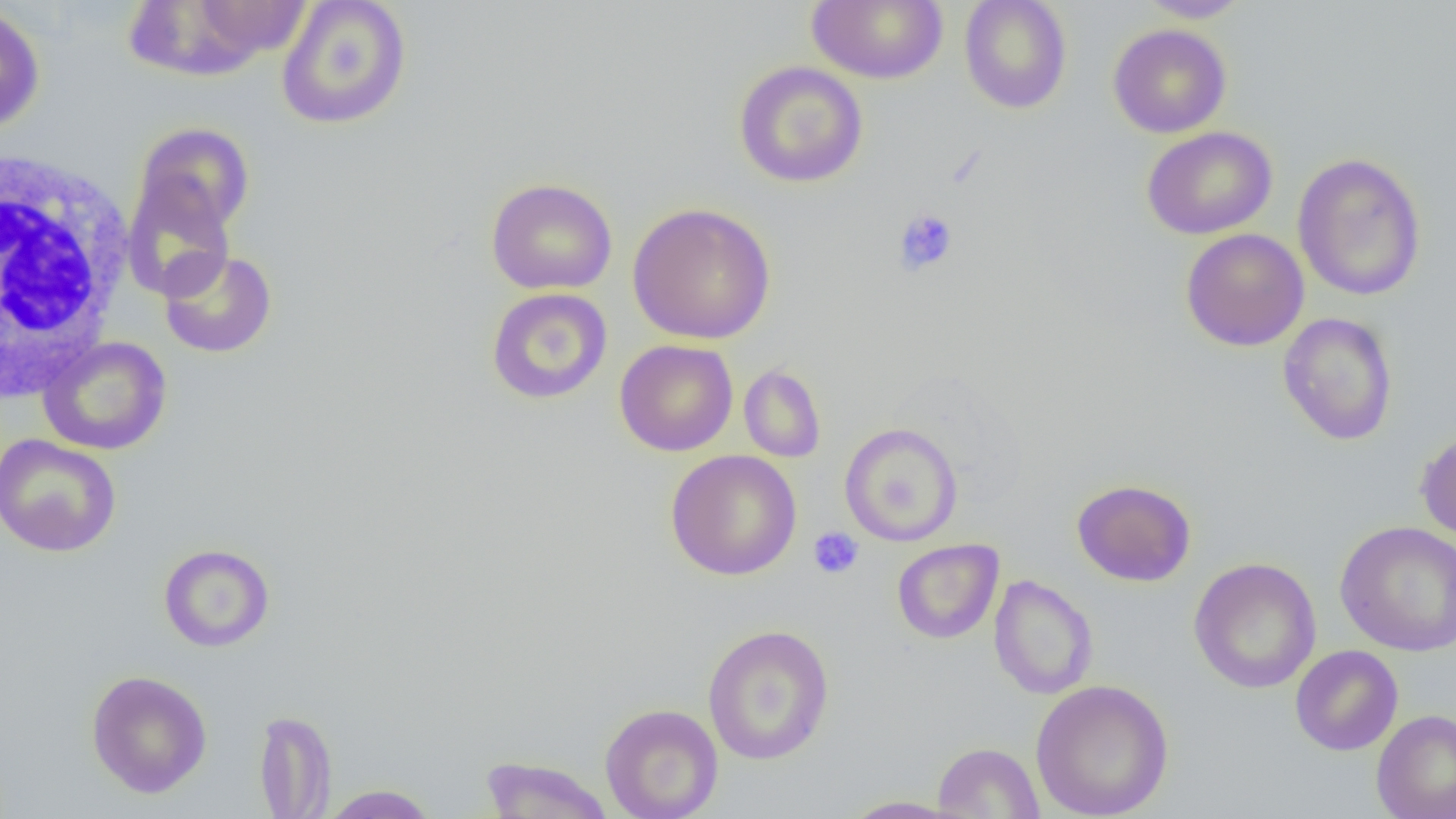
slide-level diagnosis = no evidence of blood parasites
platelet locations = approximate bounding boxes as (x1,y1)-(x2,y2) corner pairs in pixels: (893,208)-(959,277), (808,527)-(864,579)
modality = light microscopy
magnification = 1000x
uninfected red blood cell locations = approximate bounding boxes as (x1,y1)-(x2,y2) corner pairs in pixels: (276,0)-(412,130), (807,0)-(949,84), (959,0)-(1073,114), (1136,0)-(1251,22), (124,1)-(307,79), (0,4)-(45,133), (1107,23)-(1232,138), (733,61)-(868,188), (133,122)-(254,240), (1141,126)-(1277,240), (1292,152)-(1427,302), (121,171)-(237,302), (485,177)-(617,295), (627,202)-(776,345), (1180,228)-(1310,351), (158,248)-(277,358), (485,287)-(613,405), (1278,312)-(1398,446), (38,336)-(172,455), (614,339)-(738,457), (738,364)-(826,462), (839,422)-(963,546), (1415,429)-(1456,544), (0,433)-(121,558), (665,449)-(802,580), (1071,478)-(1197,587), (1336,521)-(1456,656), (892,539)-(1004,644), (158,543)-(275,652), (1188,557)-(1322,694), (988,574)-(1099,700), (702,623)-(835,766), (1289,645)-(1403,755), (85,670)-(213,798), (1031,679)-(1175,819), (600,703)-(723,819), (1371,708)-(1456,819), (254,709)-(336,818), (932,742)-(1044,818), (479,756)-(615,818), (320,784)-(440,818), (838,795)-(971,818)
image size = 1456×819 pixels
white blood cell locations = approximate bounding boxes as (x1,y1)-(x2,y2) corner pairs in pixels: (1,146)-(133,402)
preparation = thin blood smear
field of view = single